Give the preparation type.
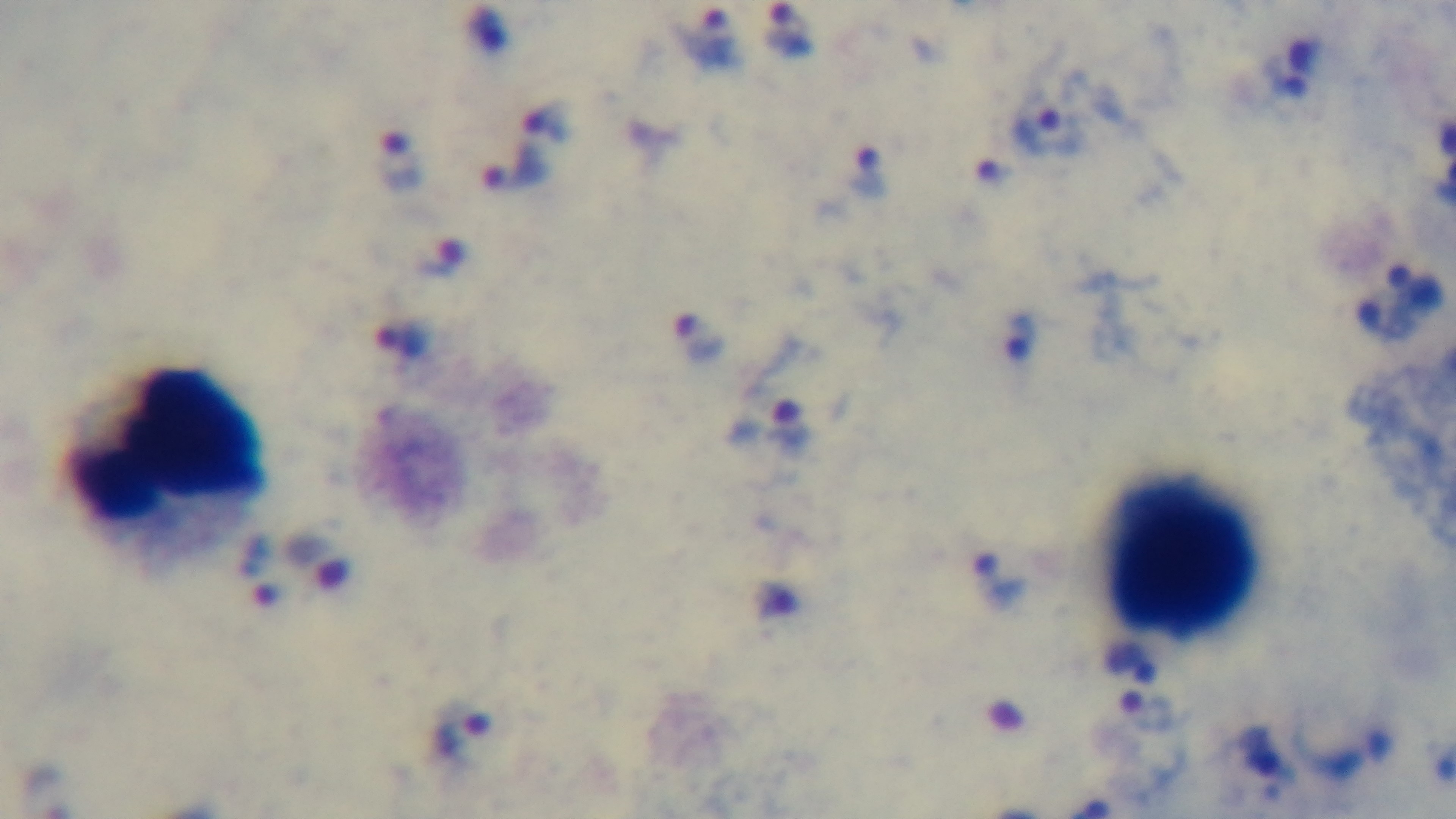
Thick.

Mounted 4K digital camera. Single field of view. 100x oil-immersion objective. Photomicrograph. Giemsa-stained. Malaria status: positive.